Assess this cell for malaria.
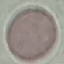

It is uninfected.

image type = cell patch, automatically extracted from a larger field of view and resized to 64 × 64 pixels
preparation = thin blood film
capture = smartphone camera at the microscope eyepiece
stain = Giemsa